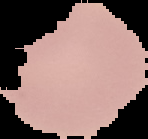

preparation = thin blood smear
image type = segmented cell region on a black background
image size = 148×139 pixels
malaria status = uninfected